Comment on the morphology of the red blood cells.
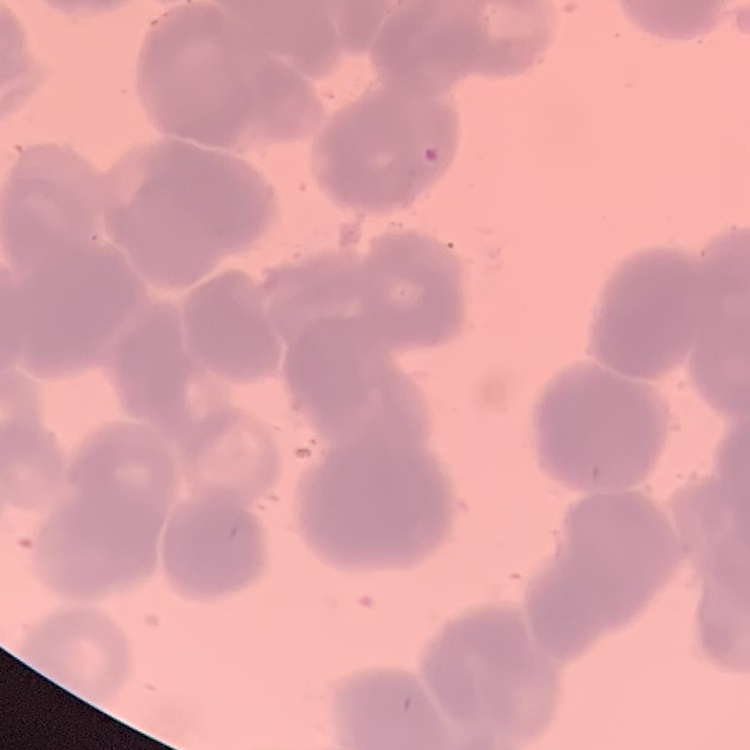
They show rouleaux formation.

Summary:
  - Image type: one tile cut from a larger photomicrograph
  - Stain: Field's or Giemsa
  - Preparation: thin blood film